Assess this cell for malaria.
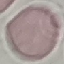

Uninfected.

Photographed with a smartphone camera at the microscope eyepiece. Thin blood film. Giemsa stain. Cell patch, automatically extracted from a larger field of view and resized to 64 × 64 pixels.